State which cell type is depicted.
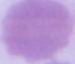

An erythrocyte.

modality = micrograph
magnification = 1000x